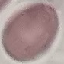
Summary:
  - Malaria status: uninfected
  - Capture: smartphone camera at the microscope eyepiece
  - Image type: automatically extracted cell patch, resized to 64 × 64 pixels
  - Stain: Giemsa
  - Preparation: thin smear